Describe the morphology of the red blood cells.
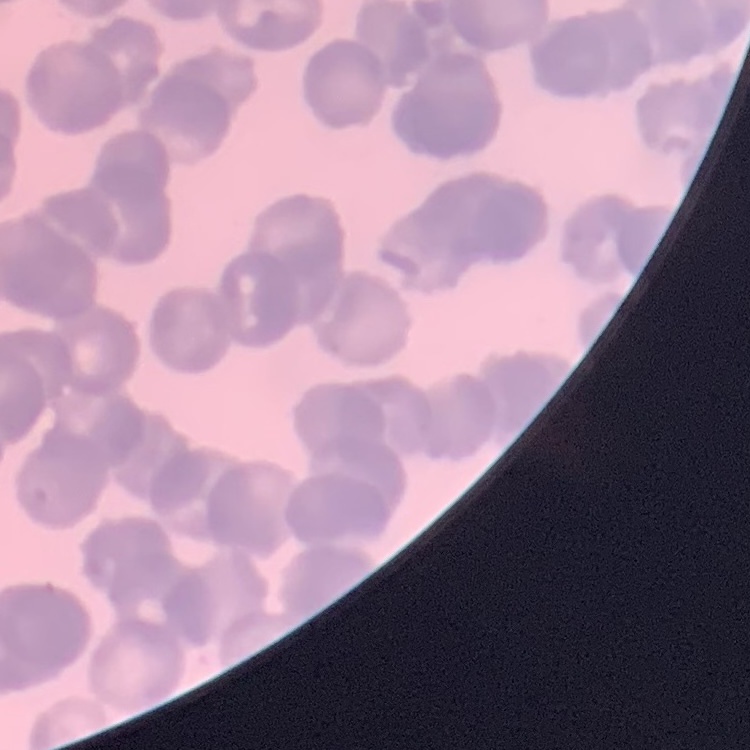
They show rouleaux formation.

One tile cut from a larger photomicrograph. Stained with either Field's or Giemsa. Thin blood film.